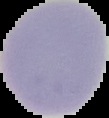
From a thin blood film. Result: no Plasmodium parasites detected. Image is 109×118 pixels. The area outside the segmented cell region is set to black.